Classify this cell by malaria status.
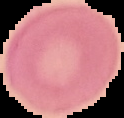

Uninfected.

{
  "image_type": "segmented cell region with the area outside set to black",
  "image_size": "124×118 pixels",
  "preparation": "thin blood smear"
}